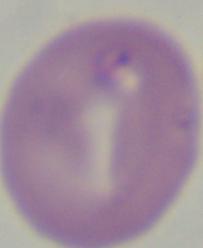
Captured at 1000x magnification. Photomicrograph. A Babesia parasite is shown.